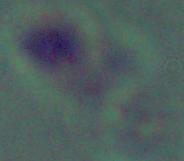

Summary:
  - Modality: micrograph
  - Identification: Leishmania
  - Magnification: 1000x